State which parasite is depicted.
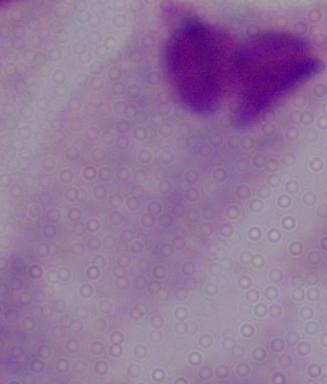
A trichomonad.

{
  "magnification": "1000x",
  "modality": "micrograph"
}